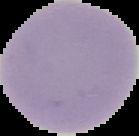

Image is 139×136 pixels. Cell region segmented out of the field of view; the surrounding area is masked to black. Malaria status: uninfected. From a thin blood film.